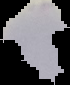 Result: no Plasmodium parasites detected. From a thin blood smear. Image is 70×85 pixels. Segmented cell region on a black background.